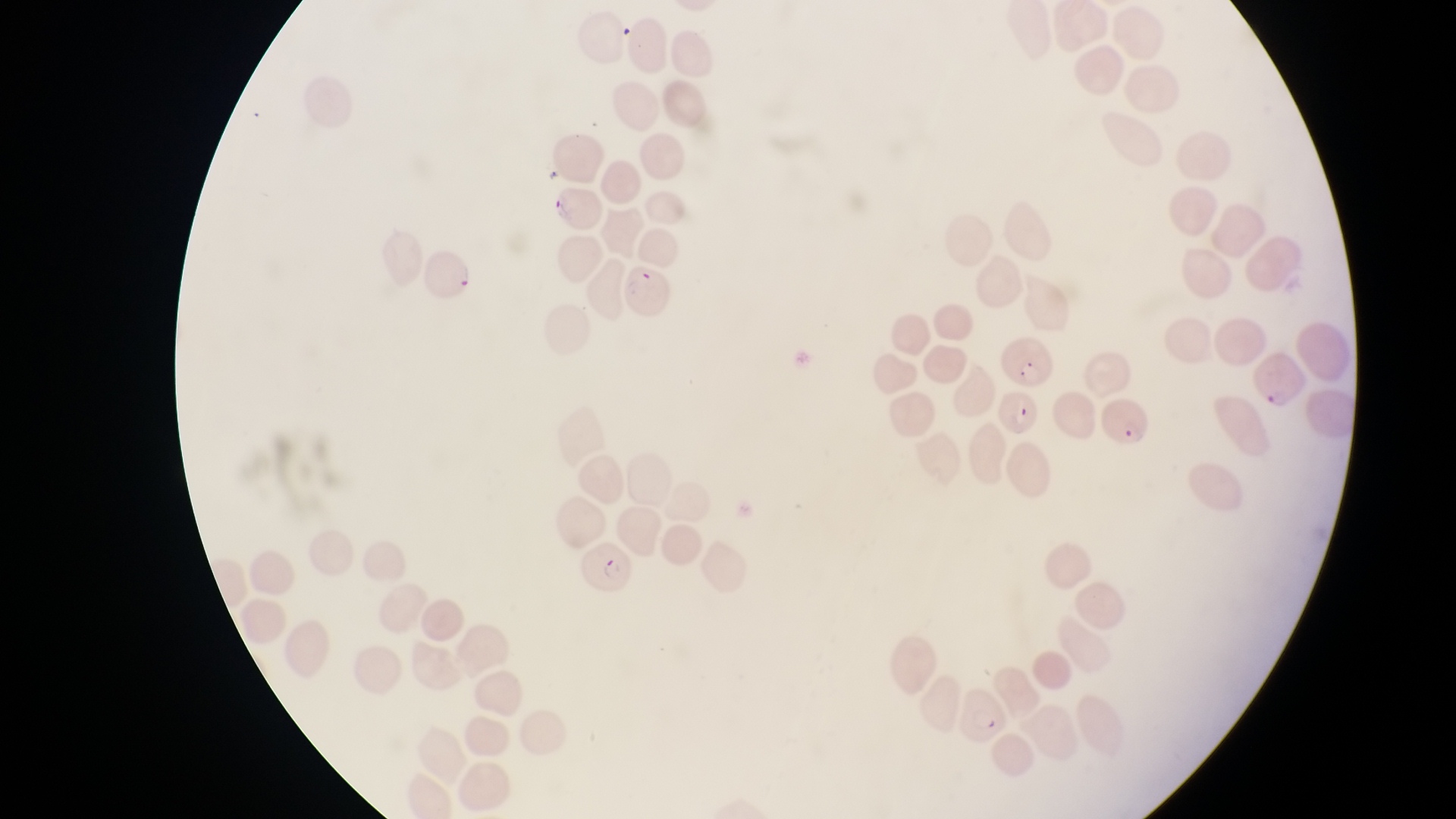
{
  "country": "Uganda",
  "capture": "smartphone photograph through the eyepiece of an Olympus CX-23 microscope",
  "preparation": "thin blood smear",
  "magnification": "1000x",
  "image_size": "1456×819 pixels",
  "field_of_view": "single",
  "parasitised_red_blood_cell_locations": "approximate bounding boxes as {left, top, right, bottom} in pixels: {544, 188, 603, 238}, {422, 248, 477, 303}, {623, 261, 676, 318}, {1003, 333, 1058, 388}, {1250, 347, 1309, 413}, {999, 389, 1039, 442}, {1099, 391, 1159, 449}, {573, 535, 642, 595}, {964, 686, 1014, 742}"
}